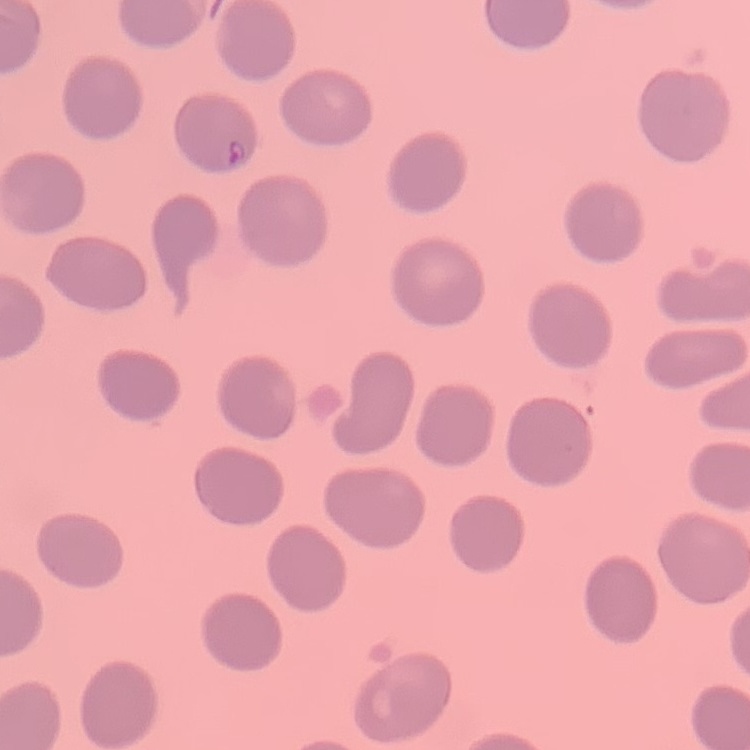
Summary:
  - Erythrocyte morphology: no rouleaux formation
  - Stain: Field's or Giemsa
  - Image type: square crop of a larger photomicrograph
  - Preparation: thin blood smear